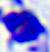 A leukocyte is shown. Micrograph. 400x magnification.